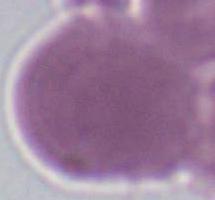

magnification = 1000x
modality = micrograph
identification = red blood cell